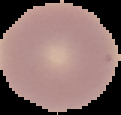

preparation: thin blood smear
image_type: segmented cell region with the area outside set to black
image_size: 121×115 pixels
result: no malaria parasites seen